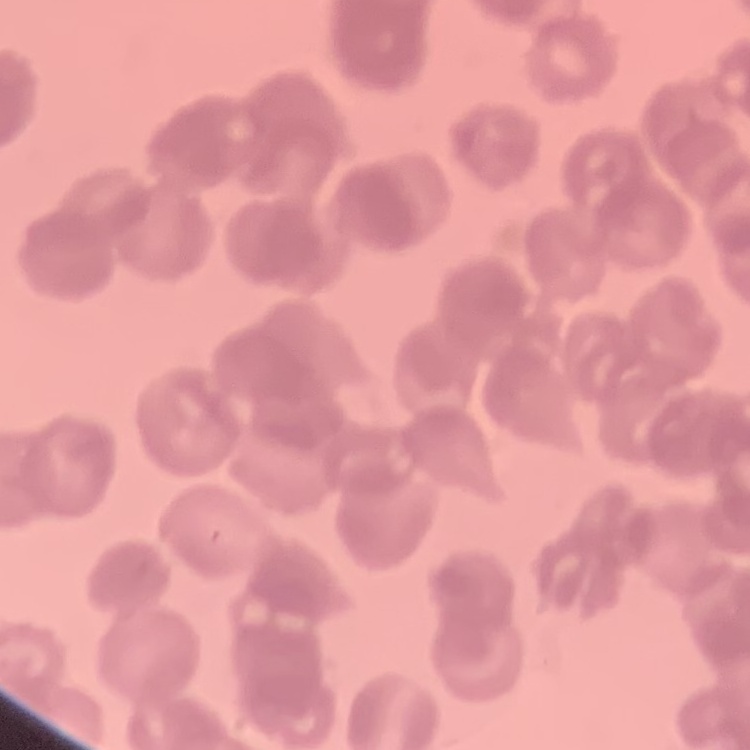

Summary:
  - Erythrocyte morphology: rouleaux formation
  - Preparation: thin peripheral smear
  - Image type: square crop of a larger photomicrograph
  - Stain: Field's or Giemsa